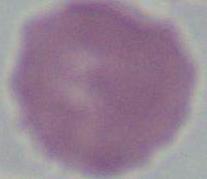

modality: micrograph
identification: erythrocyte
magnification: 1000x